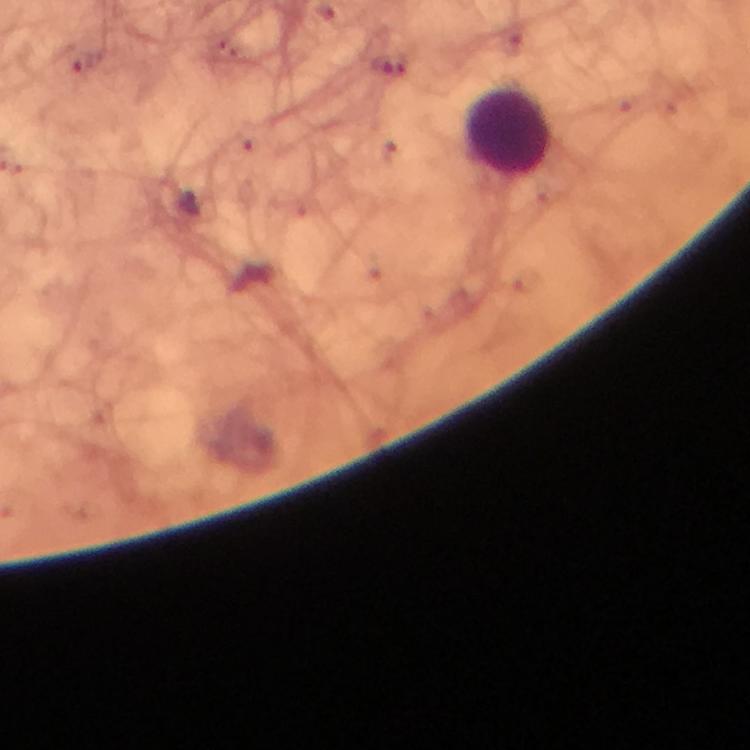
Approximate centers as {x, y} in pixels.
Summary:
  - Leukocyte locations: {510, 132}
  - Malaria parasite locations: {85, 64}, {390, 64}
  - Cropped from: one field of view
  - Stain: Giemsa
  - Context: from a malaria diagnostic workup
  - Immersion oil: applied
  - Preparation: thick blood film
  - Capture: smartphone camera through the microscope
  - Image size: 750×750 pixels
  - Magnification: 100x